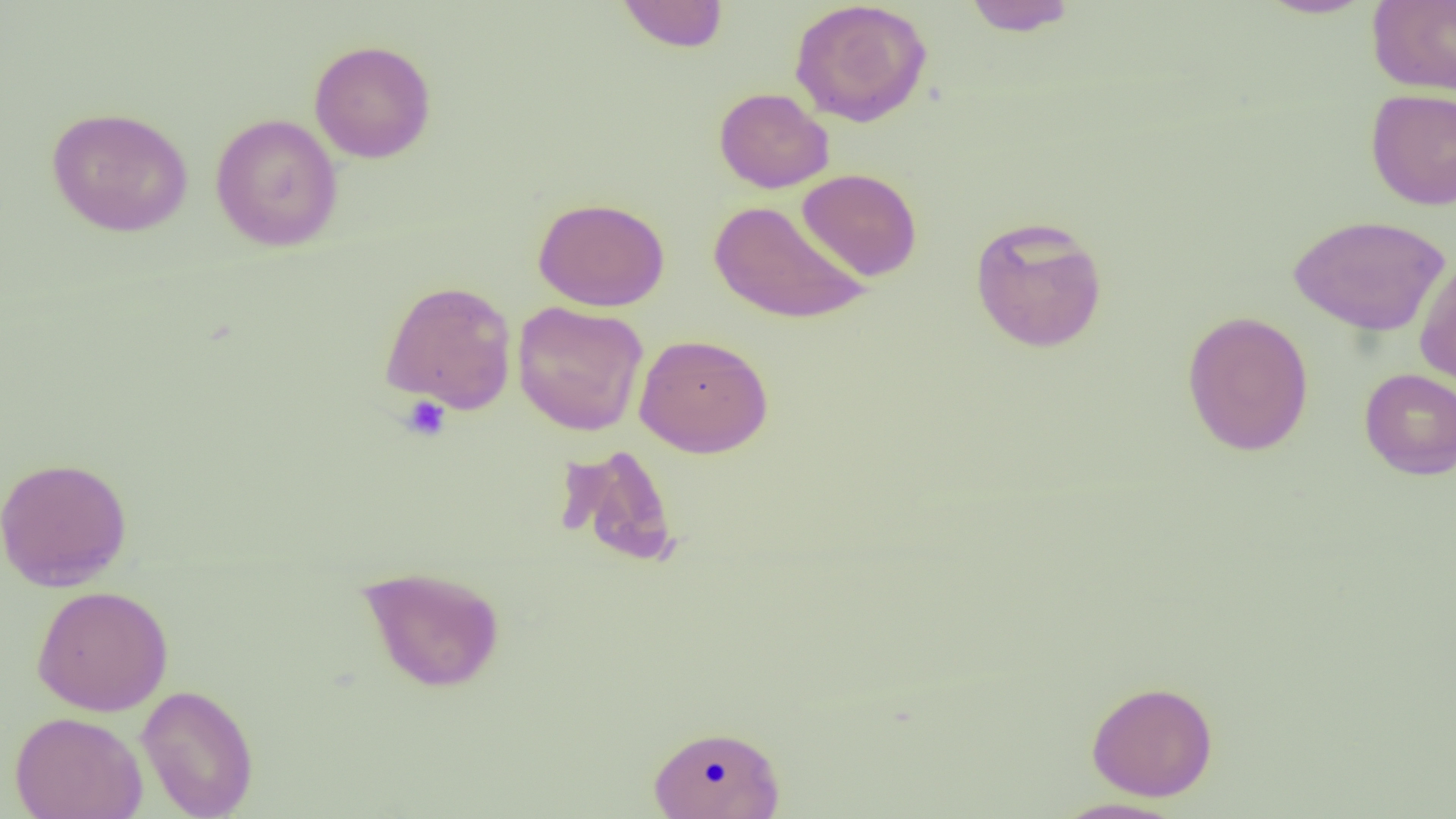
Approximate bounding boxes as (x1,y1)-(x2,y2) corner pairs in pixels. Platelet locations: (400,395)-(453,442). Uninfected red blood cell locations: (789,0)-(933,127), (962,0)-(1078,36), (1254,0)-(1377,19), (1367,0)-(1456,95), (615,1)-(730,52), (309,39)-(436,163), (713,87)-(834,193), (1365,88)-(1456,210), (46,106)-(194,237), (210,113)-(343,252), (797,168)-(922,281), (533,196)-(670,312), (709,199)-(872,325), (1288,214)-(1451,337), (969,215)-(1109,353), (1414,254)-(1456,391), (379,280)-(518,414), (512,300)-(648,435), (1181,310)-(1315,457), (634,333)-(773,457), (1359,368)-(1456,480), (555,443)-(681,569), (0,456)-(132,592), (357,564)-(506,693), (30,585)-(174,716), (1086,680)-(1218,801), (136,684)-(259,819), (10,711)-(148,819), (648,724)-(785,818), (1049,797)-(1189,818). Slide-level diagnosis: negative for blood parasites. Single field of view. Captured at 1000x magnification. Image is 1456×819 pixels. Thin blood smear. Light microscopy.